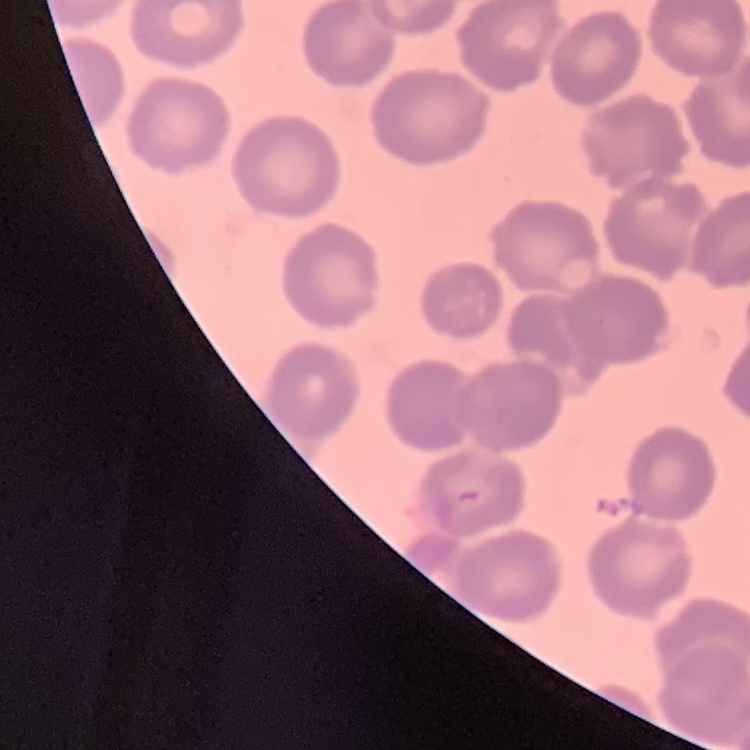

Summary:
  - Red blood cell morphology: no rouleaux formation
  - Stain: Field's or Giemsa
  - Preparation: thin blood film
  - Image type: one tile cut from a larger photomicrograph